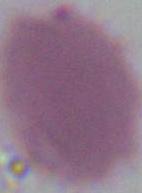

magnification: 1000x
identification: red blood cell
modality: micrograph